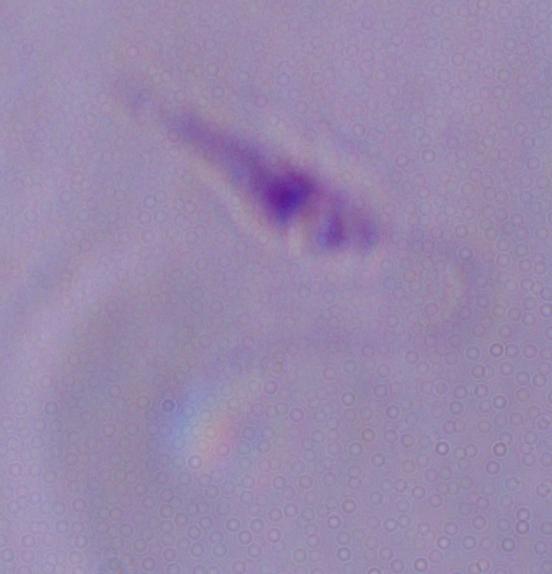 1000x magnification. A Leishmania parasite is shown. Micrograph.